Assess the morphology of the red blood cells.
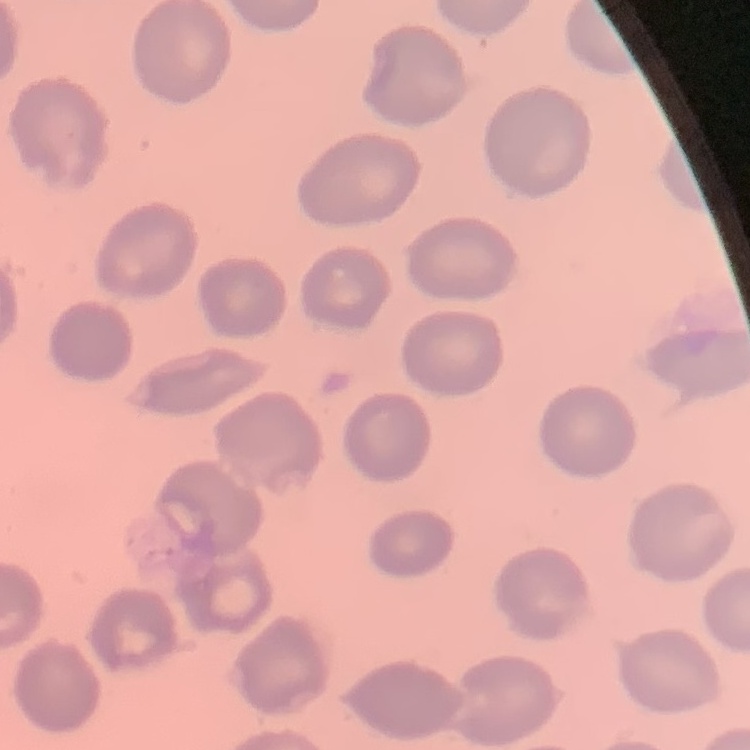

They show no rouleaux formation.

One tile cut from a larger photomicrograph. Stained with either Field's or Giemsa. Thin peripheral smear.